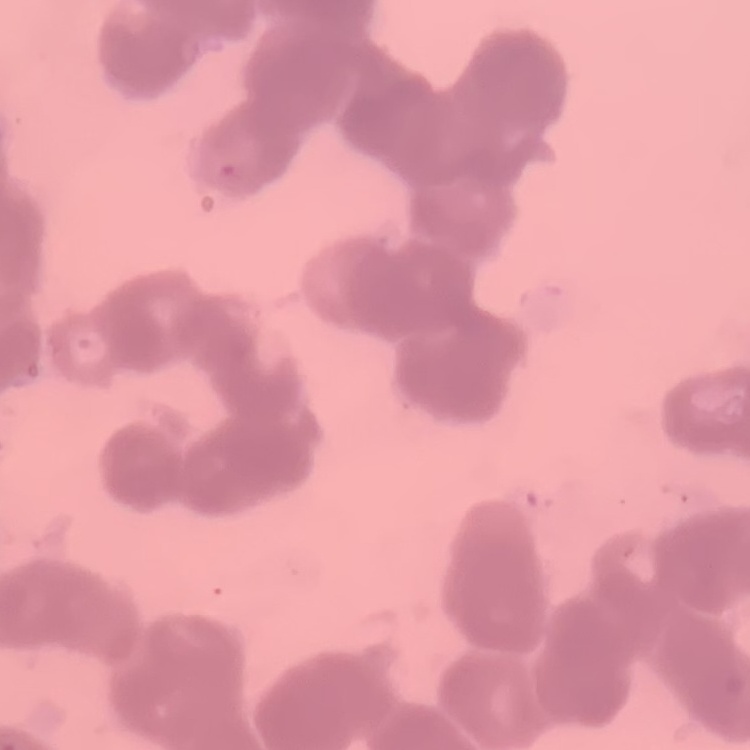

Summary:
  - Erythrocyte morphology: rouleaux formation
  - Stain: Field's or Giemsa
  - Image type: square crop of a larger photomicrograph
  - Preparation: thin blood smear